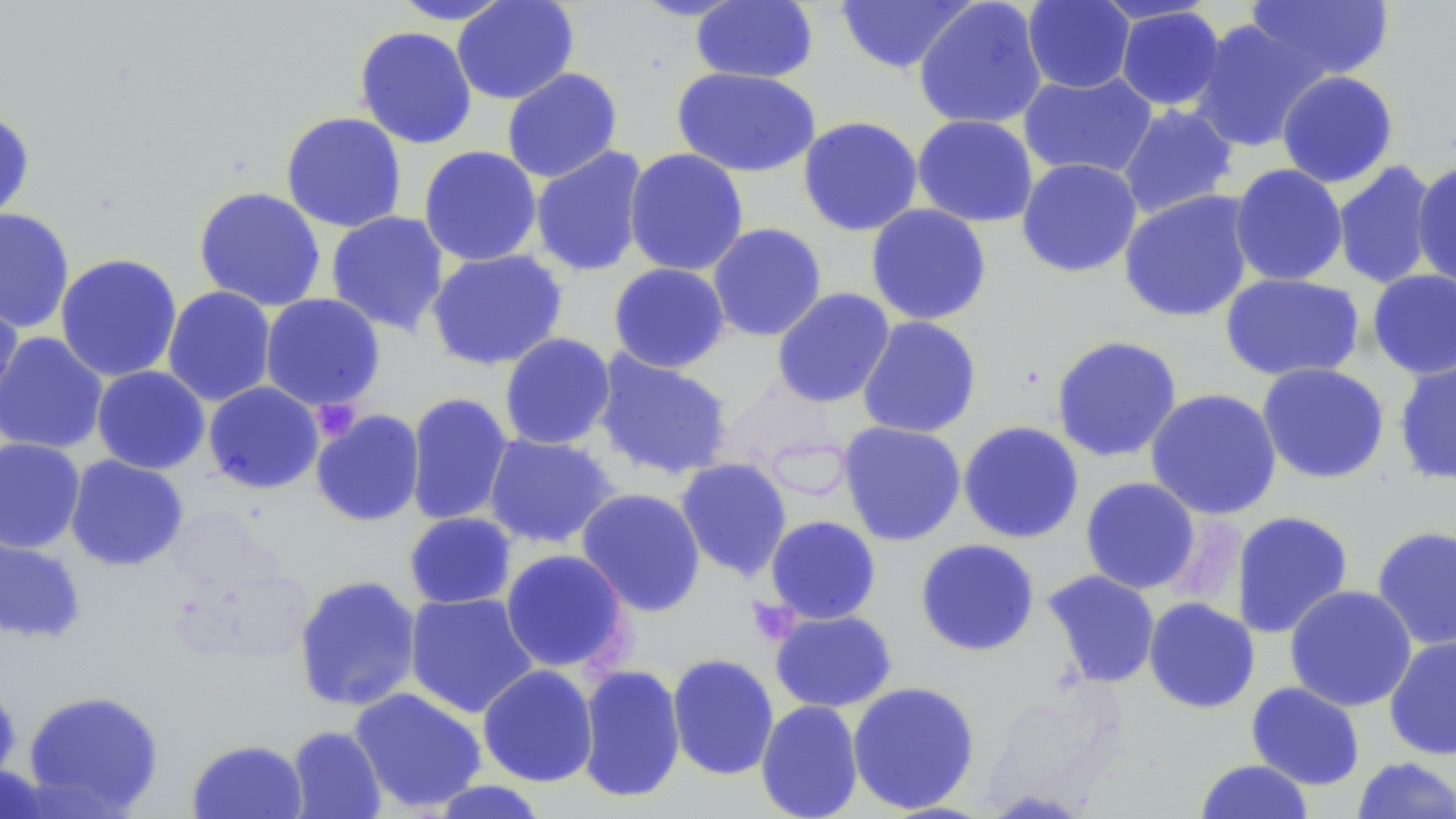
Approximate bounding boxes as (x1, y1, x2, y2) in pixels. Uninfected red blood cell locations: (388, 0, 516, 25), (451, 0, 579, 105), (631, 0, 750, 21), (1245, 0, 1396, 83), (690, 1, 819, 84), (834, 1, 977, 74), (914, 1, 1048, 129), (1022, 1, 1136, 94), (1115, 5, 1226, 111), (1188, 18, 1325, 153), (354, 25, 477, 149), (671, 67, 821, 177), (502, 68, 623, 183), (1018, 70, 1158, 180), (1276, 70, 1399, 188), (1116, 103, 1238, 220), (0, 109, 35, 223), (280, 111, 407, 233), (912, 114, 1039, 227), (797, 115, 924, 236), (418, 145, 542, 267), (530, 145, 650, 277), (623, 148, 749, 276), (1016, 157, 1143, 278), (1332, 160, 1439, 290), (1412, 161, 1456, 291), (1229, 163, 1348, 287), (193, 186, 327, 312), (1118, 190, 1255, 323), (865, 204, 993, 326), (0, 207, 75, 333), (325, 210, 450, 336), (707, 222, 827, 342), (426, 249, 569, 371), (55, 253, 183, 383), (608, 263, 730, 373), (1367, 269, 1456, 379), (1220, 272, 1365, 382), (162, 286, 277, 406), (771, 287, 896, 408), (0, 290, 24, 408), (260, 293, 386, 412), (857, 315, 982, 439), (0, 331, 109, 454), (499, 332, 616, 450), (1050, 335, 1183, 463), (592, 351, 733, 480), (1393, 353, 1456, 487), (1256, 362, 1390, 484), (91, 365, 210, 474), (203, 381, 325, 494), (1144, 388, 1282, 520), (404, 392, 514, 527), (311, 409, 425, 527), (958, 420, 1084, 544), (838, 421, 966, 546), (483, 432, 619, 550), (0, 437, 85, 553), (64, 455, 189, 571), (675, 457, 792, 581), (1080, 476, 1201, 594), (575, 487, 707, 617), (1230, 510, 1354, 639), (403, 512, 517, 609), (764, 515, 882, 624), (1371, 525, 1456, 651), (0, 532, 87, 643), (915, 538, 1040, 657), (499, 549, 632, 675), (1042, 569, 1161, 688), (293, 574, 422, 712), (1284, 584, 1417, 712), (404, 591, 539, 719), (1143, 597, 1260, 714), (769, 609, 898, 712), (1384, 633, 1456, 761), (666, 653, 780, 781), (477, 664, 598, 787), (576, 664, 686, 803), (0, 676, 22, 791), (847, 680, 981, 814), (1246, 681, 1366, 790), (349, 687, 487, 813), (22, 689, 165, 816), (755, 699, 864, 819), (287, 725, 387, 818), (186, 739, 307, 818), (1351, 757, 1456, 818), (1194, 759, 1314, 819), (0, 764, 58, 819), (429, 780, 550, 818). Platelet locations: (312, 400, 363, 439), (748, 596, 800, 639). Slide-level diagnosis: no evidence of blood parasites. Thin blood film. Captured at 1000x magnification. One field of a larger specimen. Light microscopy. Image is 1456×819 pixels. May-Grünwald-Giemsa-stained preparation.